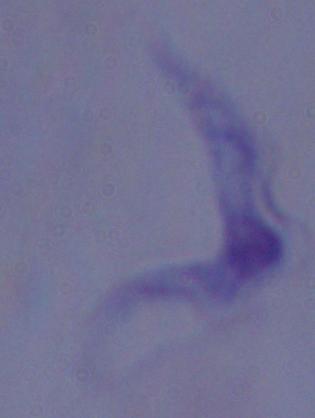

Summary:
  - Modality: photomicrograph
  - Magnification: 1000x
  - Identification: trypanosome